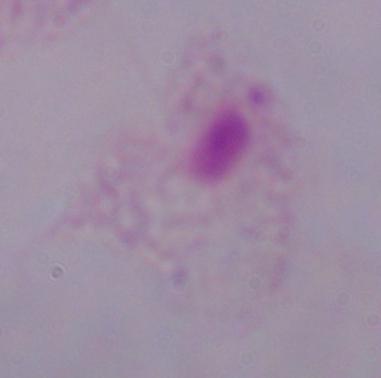

A trichomonad is shown. Micrograph. 1000x magnification.